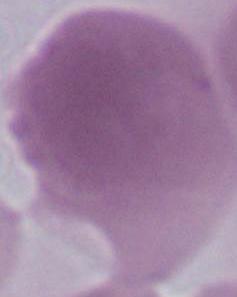

modality = photomicrograph
identification = red blood cell
magnification = 1000x